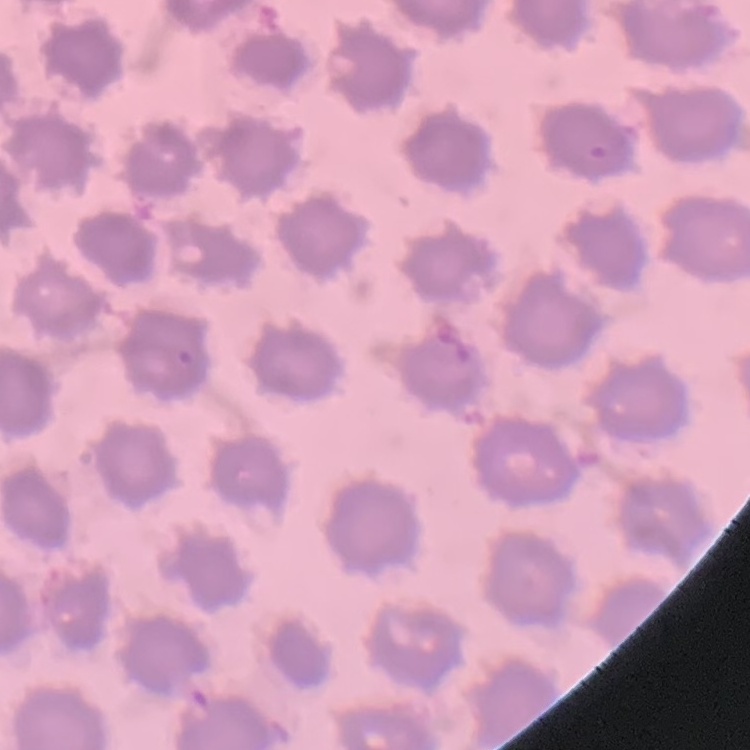

Summary:
  - Red blood cell morphology: no rouleaux formation
  - Preparation: thin peripheral smear
  - Image type: square crop of a larger photomicrograph
  - Stain: Field's or Giemsa